Outline each blood parasite and name the species.
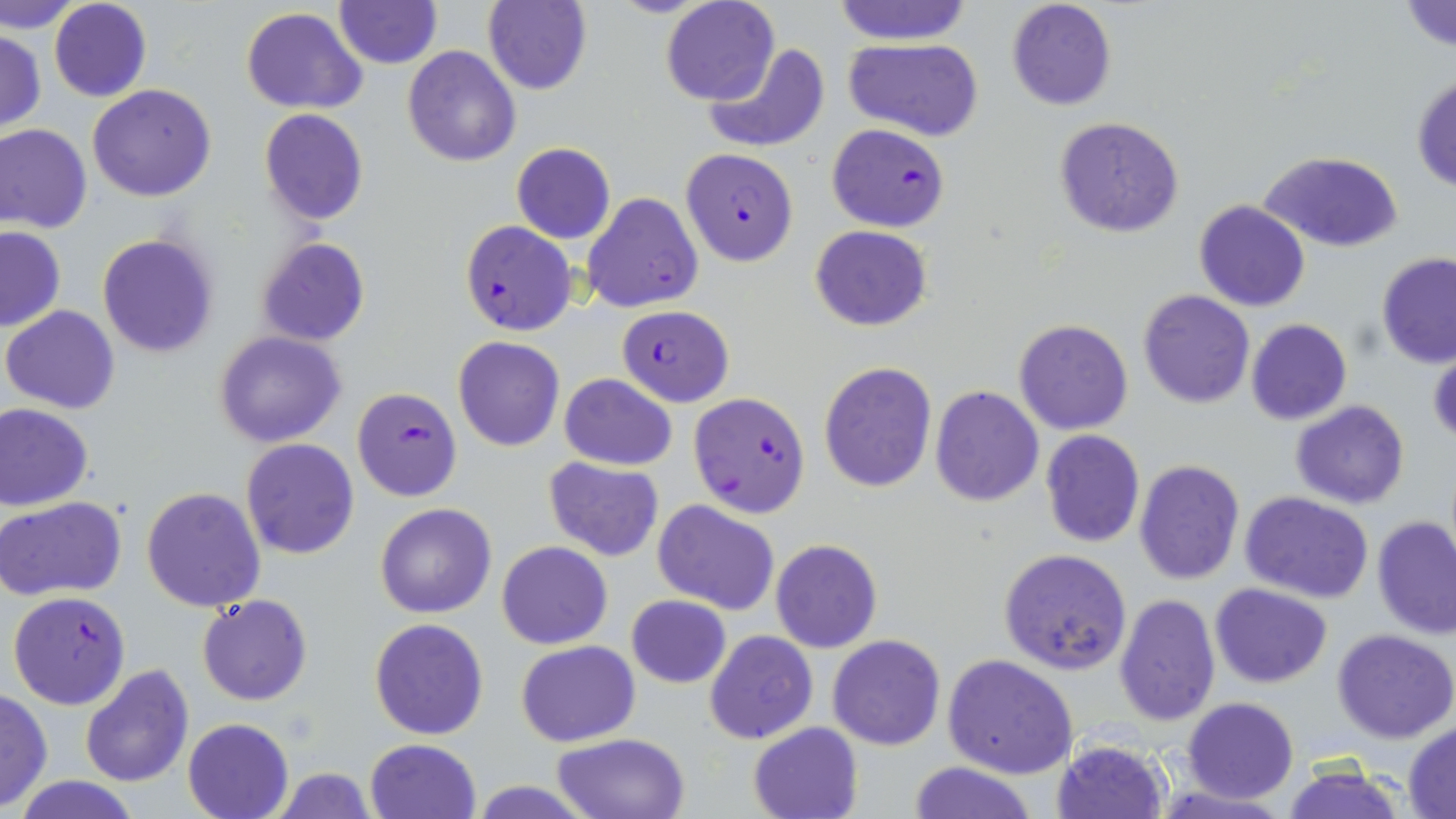

Approximate bounding boxes as named x1/y1/x2/y2 corners in pixels.
Plasmodium falciparum-infected red blood cells: (x1=826, y1=124, x2=950, y2=232), (x1=679, y1=147, x2=799, y2=266), (x1=458, y1=220, x2=578, y2=336), (x1=618, y1=305, x2=733, y2=406), (x1=352, y1=388, x2=462, y2=502), (x1=687, y1=392, x2=811, y2=519), (x1=7, y1=591, x2=131, y2=711).
No Plasmodium ovale, Plasmodium malariae, Plasmodium vivax, Babesia divergens, or Trypanosoma brucei observed.

slide-level diagnosis = Plasmodium falciparum
stain = May-Grünwald-Giemsa
magnification = 1000x
preparation = thin blood film
field of view = one of a larger specimen
uninfected red blood cell locations = approximate bounding boxes as named x1/y1/x2/y2 corners in pixels: (x1=3, y1=0, x2=82, y2=34), (x1=48, y1=0, x2=153, y2=102), (x1=660, y1=0, x2=781, y2=106), (x1=1006, y1=0, x2=1117, y2=112), (x1=1400, y1=0, x2=1456, y2=54), (x1=334, y1=1, x2=440, y2=69), (x1=483, y1=1, x2=593, y2=95), (x1=830, y1=1, x2=976, y2=45), (x1=241, y1=8, x2=367, y2=113), (x1=1, y1=31, x2=47, y2=133), (x1=844, y1=37, x2=985, y2=142), (x1=702, y1=43, x2=831, y2=155), (x1=402, y1=45, x2=521, y2=166), (x1=1411, y1=73, x2=1456, y2=194), (x1=86, y1=83, x2=217, y2=202), (x1=259, y1=109, x2=368, y2=225), (x1=1053, y1=117, x2=1186, y2=238), (x1=0, y1=124, x2=93, y2=234), (x1=511, y1=142, x2=616, y2=244), (x1=1260, y1=151, x2=1403, y2=252), (x1=582, y1=192, x2=704, y2=313), (x1=1194, y1=200, x2=1310, y2=312), (x1=810, y1=225, x2=931, y2=331), (x1=0, y1=227, x2=66, y2=332), (x1=97, y1=235, x2=218, y2=358), (x1=254, y1=236, x2=371, y2=348), (x1=1376, y1=253, x2=1456, y2=368), (x1=1137, y1=290, x2=1255, y2=409), (x1=3, y1=305, x2=120, y2=414), (x1=1014, y1=318, x2=1133, y2=435), (x1=1246, y1=318, x2=1352, y2=425), (x1=213, y1=331, x2=348, y2=448), (x1=453, y1=335, x2=565, y2=452), (x1=1428, y1=346, x2=1455, y2=446), (x1=818, y1=361, x2=938, y2=493), (x1=559, y1=373, x2=678, y2=471), (x1=929, y1=385, x2=1044, y2=507), (x1=1289, y1=401, x2=1411, y2=509), (x1=0, y1=402, x2=94, y2=511), (x1=1041, y1=430, x2=1145, y2=547), (x1=241, y1=438, x2=359, y2=558), (x1=544, y1=456, x2=665, y2=562), (x1=1134, y1=459, x2=1246, y2=586), (x1=141, y1=486, x2=268, y2=611), (x1=1239, y1=492, x2=1375, y2=603), (x1=0, y1=495, x2=129, y2=602), (x1=652, y1=501, x2=780, y2=614), (x1=374, y1=502, x2=497, y2=618), (x1=1372, y1=517, x2=1456, y2=639), (x1=770, y1=539, x2=882, y2=653), (x1=497, y1=541, x2=613, y2=649), (x1=998, y1=549, x2=1132, y2=676), (x1=1209, y1=582, x2=1332, y2=687), (x1=1115, y1=592, x2=1221, y2=727), (x1=197, y1=594, x2=312, y2=705), (x1=626, y1=594, x2=730, y2=689), (x1=370, y1=617, x2=489, y2=739), (x1=704, y1=629, x2=818, y2=745), (x1=1333, y1=629, x2=1456, y2=744), (x1=828, y1=634, x2=945, y2=751), (x1=516, y1=640, x2=639, y2=748), (x1=942, y1=653, x2=1079, y2=778), (x1=79, y1=664, x2=194, y2=788), (x1=0, y1=687, x2=51, y2=811), (x1=1184, y1=698, x2=1297, y2=803), (x1=183, y1=717, x2=294, y2=819), (x1=748, y1=721, x2=863, y2=819), (x1=1404, y1=724, x2=1455, y2=816), (x1=552, y1=732, x2=691, y2=819), (x1=365, y1=738, x2=481, y2=819), (x1=1051, y1=739, x2=1171, y2=819), (x1=906, y1=760, x2=1038, y2=819), (x1=1282, y1=764, x2=1406, y2=819), (x1=274, y1=766, x2=377, y2=819), (x1=8, y1=776, x2=149, y2=818), (x1=467, y1=781, x2=598, y2=817), (x1=1148, y1=783, x2=1297, y2=819)
image size = 1456×819 pixels
modality = light microscopy